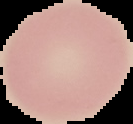

image type = segmented cell region with the area outside set to black
preparation = thin blood film
image size = 133×124 pixels
result = no malaria parasites detected